Name the parasite shown.
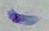
This is Toxoplasma gondii.

Photomicrograph. Captured at 1000x magnification.